State the preparation type.
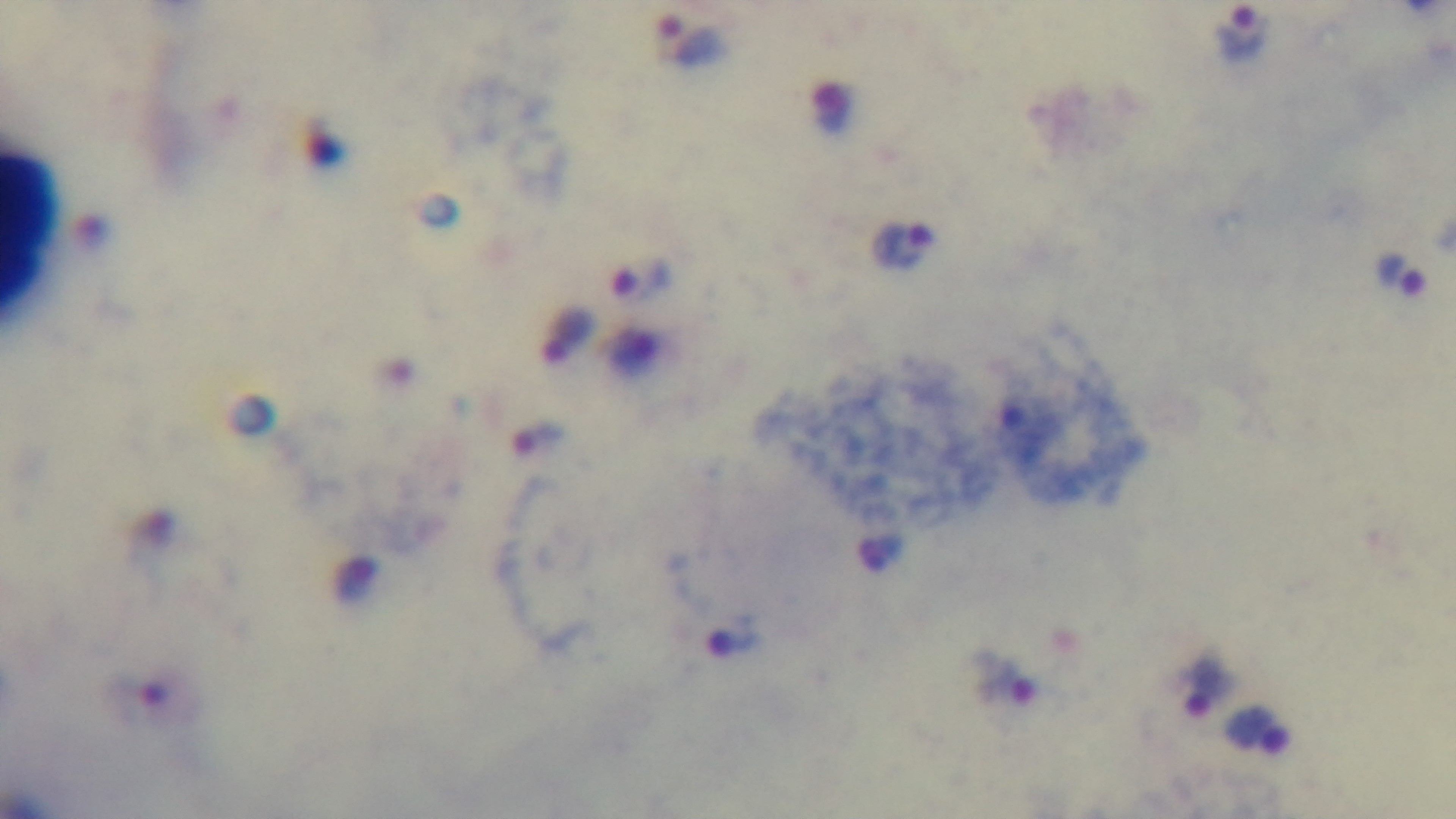

It is a thick blood film.

Photomicrograph. One field from the slide. Oil-immersion objective, 100x. Malaria status: positive. Giemsa stain. Captured with a mounted 4K digital camera.